Describe the morphology of the red blood cells.
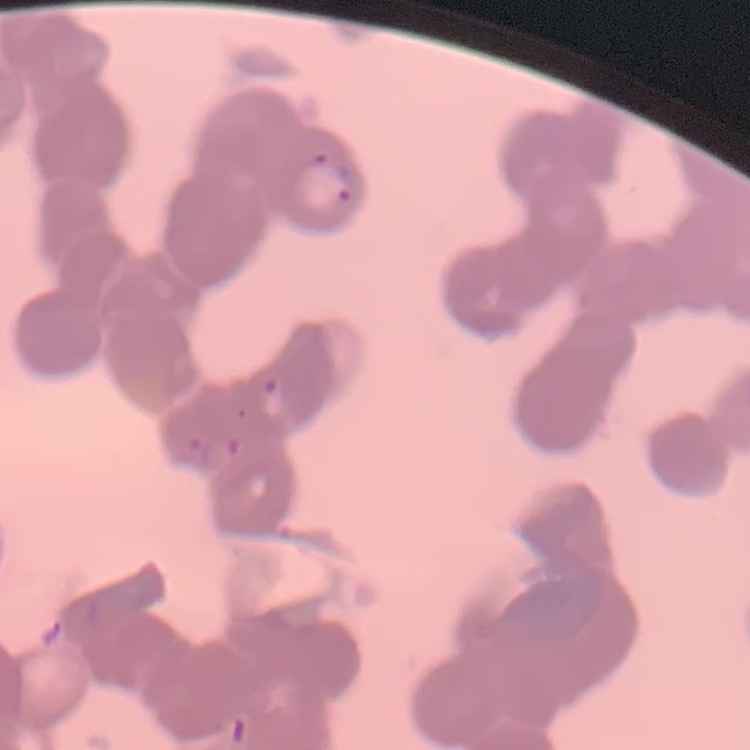
They show rouleaux formation.

stain = Field's or Giemsa
image type = square crop of a larger photomicrograph
preparation = thin peripheral smear